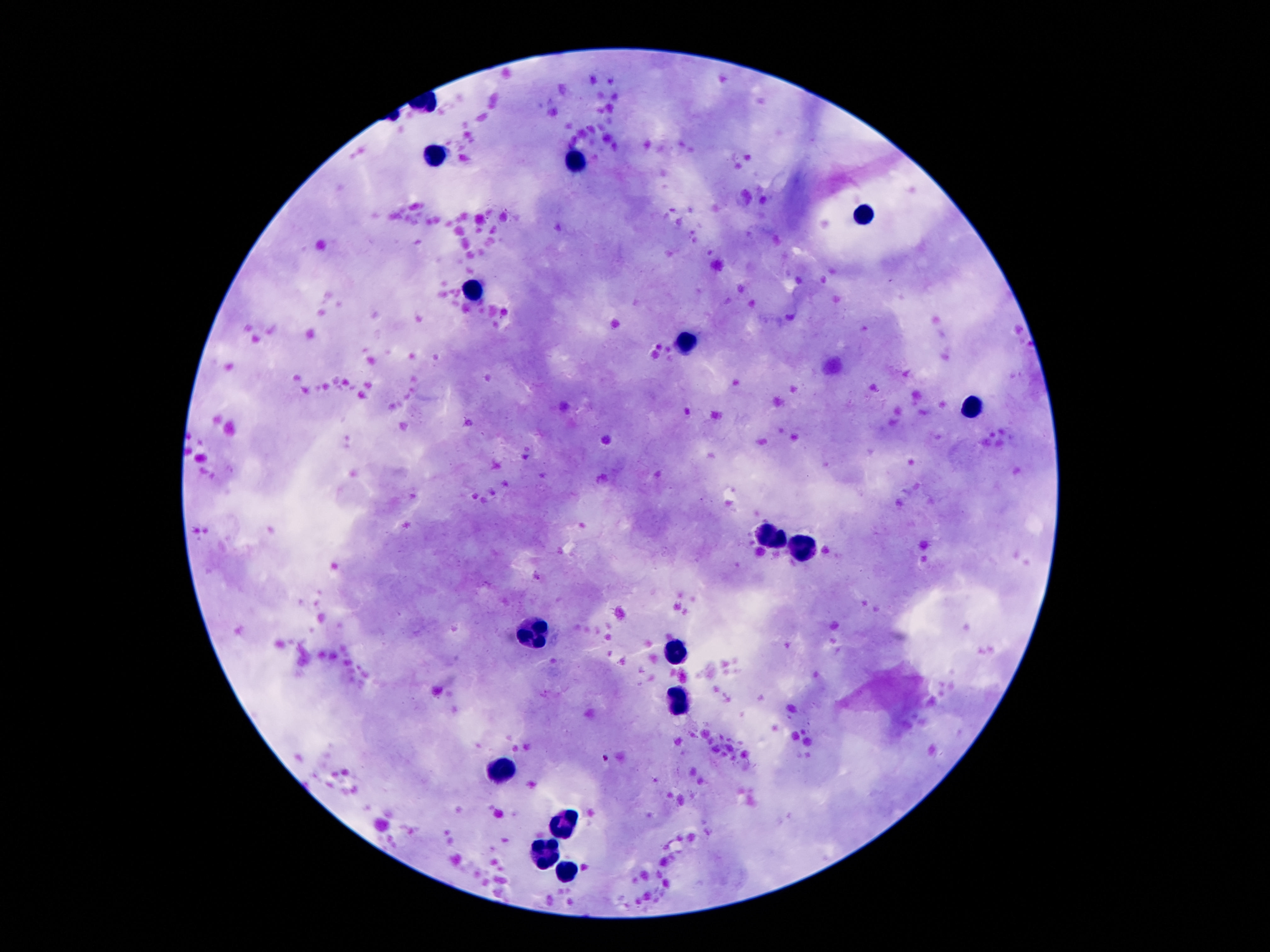
patient_malaria_status: uninfected
leukocyte_locations: 'approximate centers as [x, y] in pixels: [438, 154], [576, 160], [867, 213], [476, 289], [686, 340], [976, 404], [774, 534], [803, 553], [535, 633], [679, 649], [679, 699], [502, 764], [563, 819], [545, 855], [567, 872]'
image_size: 1270×952 pixels
stain: Giemsa
magnification: 100x
field_of_view: single
preparation: thick blood smear
capture: smartphone camera through the microscope eyepiece